Outline each blood parasite and name the species.
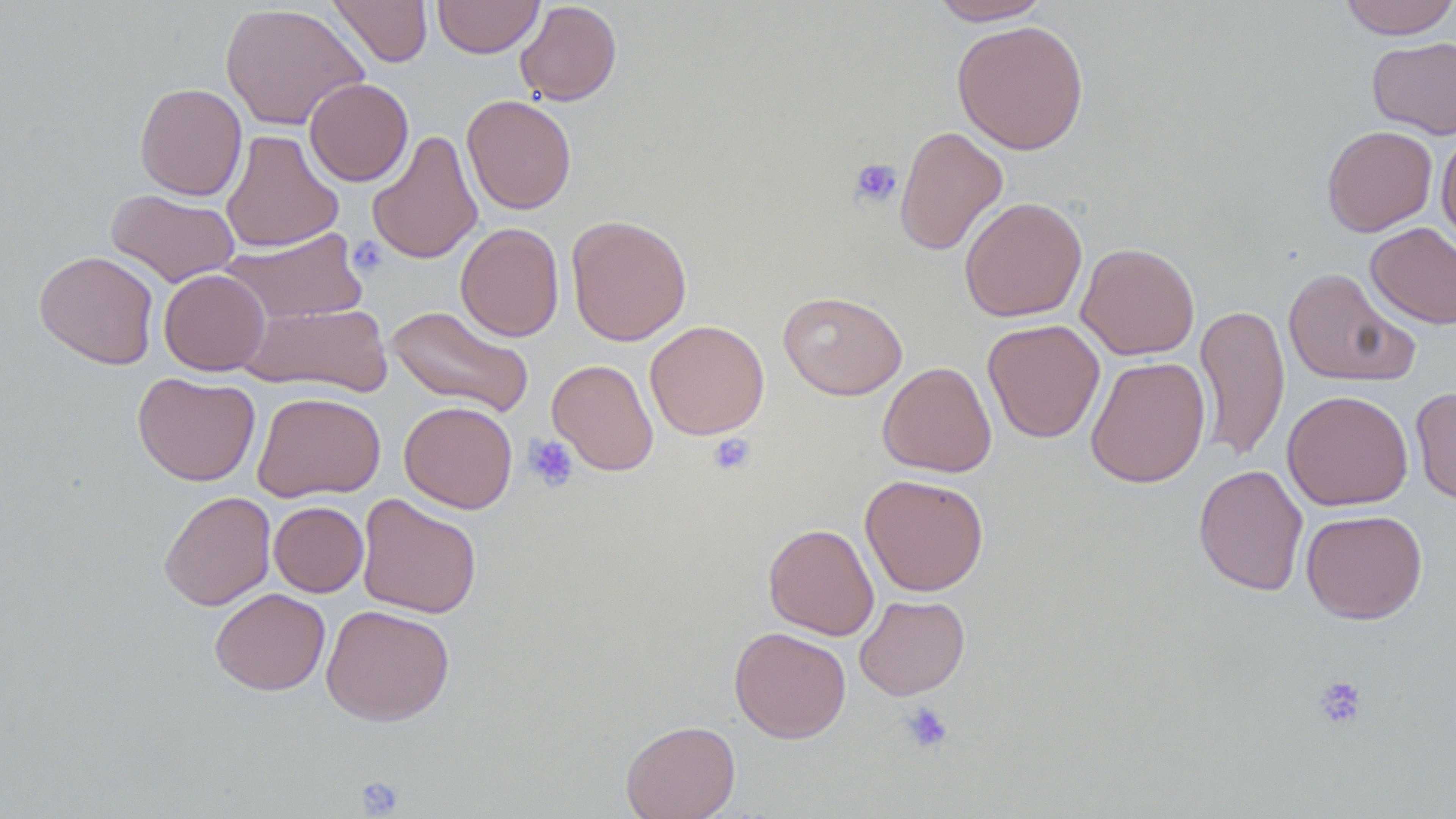
No blood parasites seen.

Summary:
  - Coordinate format: approximate bounding boxes as (x1,y1)-(x2,y2) corner pairs in pixels
  - Platelet locations: (849,158)-(902,208), (347,235)-(388,278), (708,433)-(755,475), (523,435)-(579,492), (1312,675)-(1367,729), (900,701)-(954,754), (355,775)-(405,817)
  - Uninfected red blood cell locations: (328,0)-(433,68), (433,0)-(543,58), (929,0)-(1051,24), (1337,0)-(1456,39), (515,1)-(622,106), (220,3)-(368,131), (951,19)-(1090,154), (1367,36)-(1456,139), (304,78)-(413,186), (134,82)-(247,200), (462,95)-(576,215), (894,125)-(1009,256), (1322,125)-(1437,236), (221,129)-(344,253), (1436,129)-(1456,251), (367,130)-(483,265), (106,189)-(240,287), (959,196)-(1087,322), (566,213)-(692,347), (455,222)-(565,341), (1365,222)-(1456,329), (221,228)-(368,326), (1076,242)-(1200,360), (34,250)-(159,369), (1283,267)-(1417,387), (159,269)-(270,376), (778,290)-(908,400), (241,301)-(392,396), (386,304)-(533,418), (1195,304)-(1290,463), (983,319)-(1105,443), (644,320)-(769,440), (1085,356)-(1211,489), (547,358)-(659,476), (877,361)-(997,478), (133,371)-(261,486), (1410,386)-(1456,505), (1281,389)-(1413,511), (252,391)-(386,502), (399,400)-(518,513), (1193,464)-(1308,596), (859,474)-(989,597), (158,490)-(276,610), (357,493)-(482,619), (269,501)-(368,597), (1301,509)-(1428,624), (763,522)-(880,640), (210,588)-(330,695), (854,595)-(970,700), (321,604)-(455,726), (729,625)-(851,743), (621,719)-(740,819)
  - Slide-level diagnosis: no evidence of blood parasites
  - Preparation: thin blood smear
  - Stain: May-Grünwald-Giemsa
  - Image size: 1456×819 pixels
  - Field of view: one of a larger specimen
  - Magnification: 1000x
  - Modality: optical microscopy